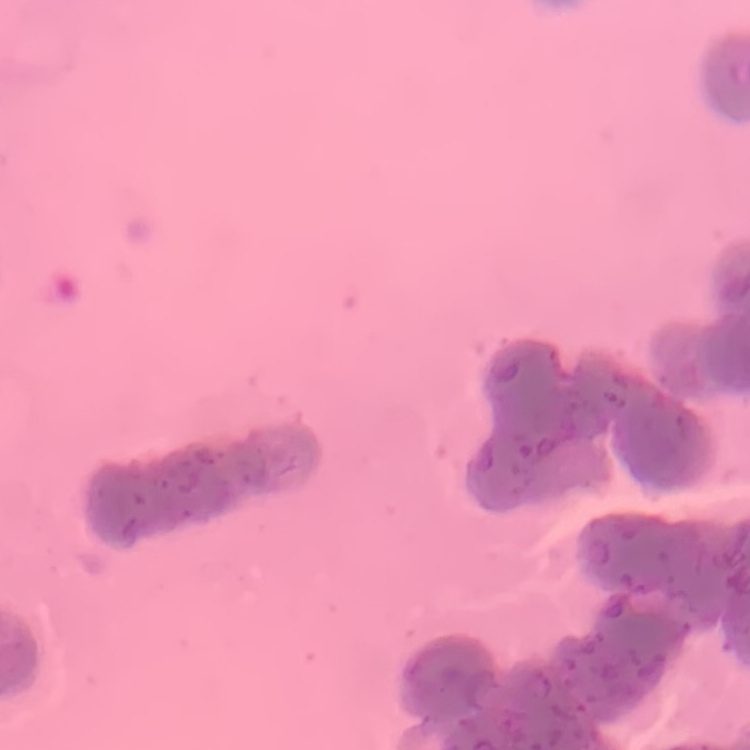

The red blood cells show rouleaux formation. Stained with either Field's or Giemsa. Thin peripheral smear. Square crop of a larger photomicrograph.